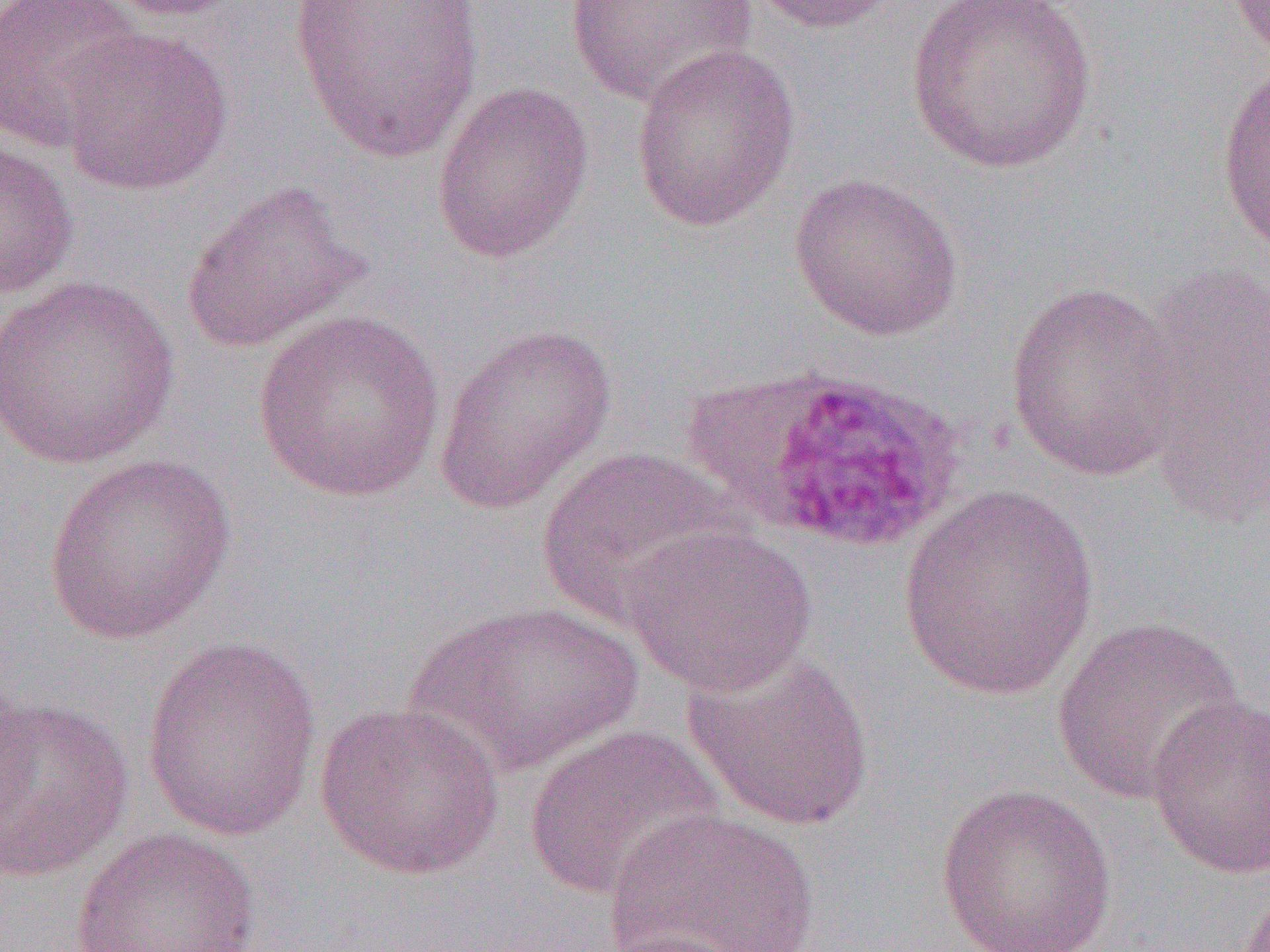
slide-level diagnosis = Plasmodium ovale
preparation = thin blood film
uninfected red blood cell locations = approximate bounding boxes as (x1,y1)-(x2,y2) corner pairs in pixels: (0,0)-(144,152), (93,0)-(251,21), (289,0)-(486,164), (563,0)-(757,107), (740,0)-(906,35), (905,0)-(1101,174), (1225,1)-(1270,61), (59,26)-(233,196), (629,41)-(800,231), (1215,58)-(1270,257), (431,80)-(594,264), (0,139)-(79,300), (788,171)-(964,341), (180,178)-(372,353), (1134,256)-(1270,526), (0,273)-(181,470), (1006,280)-(1183,480), (251,309)-(446,503), (434,321)-(617,516), (535,446)-(744,627), (42,452)-(236,645), (899,484)-(1100,702), (620,523)-(818,696), (402,596)-(648,777), (1051,614)-(1247,805), (140,636)-(322,842), (681,649)-(877,832), (0,691)-(134,882), (1146,693)-(1270,878), (313,700)-(505,880), (523,722)-(726,901), (934,782)-(1119,952), (601,808)-(821,952), (70,827)-(262,951)
magnification = 1000x
image size = 1270×952 pixels
field of view = single
modality = optical microscopy